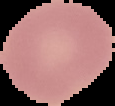

Image is 115×106 pixels. From a thin blood film. Malaria status: uninfected. Cell region segmented out of the field of view; the surrounding area is masked to black.